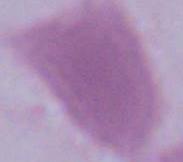

identification = erythrocyte
magnification = 1000x
modality = photomicrograph